Classify this cell by malaria status.
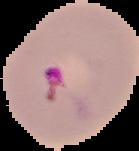
Parasitized.

image_type: cell region segmented out of the field of view; surrounding area masked to black
image_size: 139×151 pixels
preparation: thin blood smear